Locate every Plasmodium falciparum-infected red blood cell.
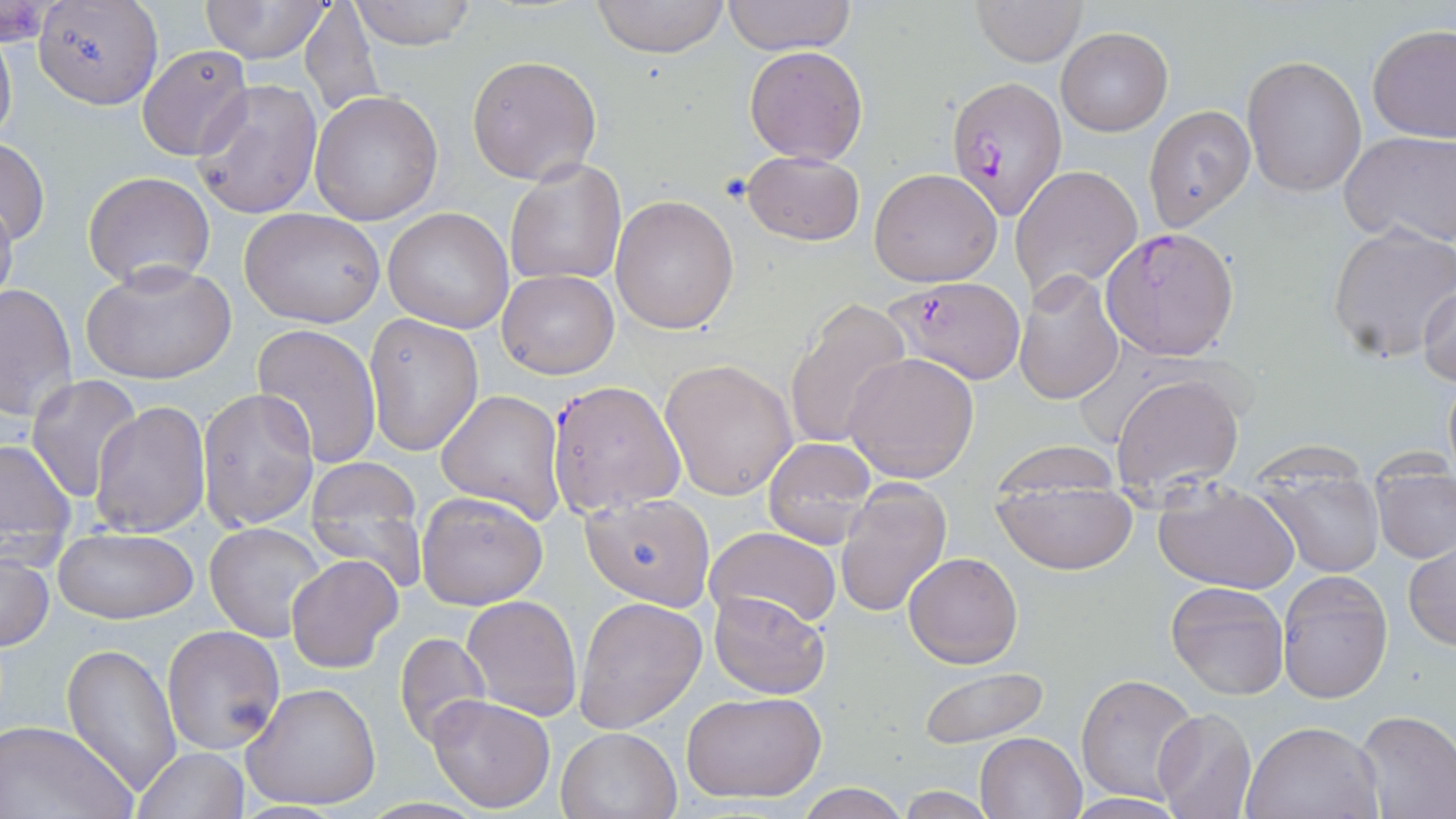

Approximate bounding boxes as named x1/y1/x2/y2 corners in pixels.
Plasmodium falciparum-infected red blood cells: (x1=944, y1=74, x2=1068, y2=220), (x1=1101, y1=226, x2=1241, y2=361), (x1=883, y1=276, x2=1027, y2=385), (x1=547, y1=380, x2=685, y2=516).

Uninfected red blood cell locations: (x1=197, y1=0, x2=333, y2=64), (x1=347, y1=0, x2=478, y2=50), (x1=591, y1=0, x2=731, y2=58), (x1=724, y1=0, x2=856, y2=54), (x1=973, y1=0, x2=1087, y2=66), (x1=33, y1=2, x2=162, y2=109), (x1=298, y1=2, x2=382, y2=116), (x1=0, y1=26, x2=17, y2=157), (x1=1368, y1=26, x2=1456, y2=145), (x1=1056, y1=28, x2=1172, y2=135), (x1=744, y1=45, x2=869, y2=166), (x1=137, y1=46, x2=252, y2=159), (x1=466, y1=54, x2=602, y2=184), (x1=1242, y1=55, x2=1366, y2=197), (x1=192, y1=78, x2=321, y2=219), (x1=310, y1=90, x2=442, y2=226), (x1=1142, y1=105, x2=1255, y2=230), (x1=1340, y1=131, x2=1456, y2=247), (x1=0, y1=138, x2=51, y2=249), (x1=741, y1=149, x2=866, y2=247), (x1=503, y1=156, x2=628, y2=285), (x1=1012, y1=164, x2=1142, y2=300), (x1=869, y1=167, x2=1002, y2=287), (x1=83, y1=171, x2=216, y2=288), (x1=0, y1=185, x2=18, y2=317), (x1=610, y1=195, x2=740, y2=334), (x1=239, y1=207, x2=385, y2=329), (x1=382, y1=207, x2=513, y2=333), (x1=1327, y1=223, x2=1456, y2=363), (x1=81, y1=260, x2=236, y2=385), (x1=495, y1=269, x2=618, y2=380), (x1=1014, y1=269, x2=1124, y2=405), (x1=1, y1=283, x2=77, y2=423), (x1=1418, y1=284, x2=1455, y2=384), (x1=783, y1=297, x2=911, y2=450), (x1=364, y1=312, x2=483, y2=456), (x1=252, y1=324, x2=381, y2=469), (x1=844, y1=352, x2=980, y2=484), (x1=661, y1=359, x2=798, y2=501), (x1=1441, y1=366, x2=1455, y2=484), (x1=1110, y1=371, x2=1244, y2=499), (x1=26, y1=375, x2=143, y2=503), (x1=198, y1=387, x2=319, y2=534), (x1=435, y1=389, x2=566, y2=524), (x1=90, y1=400, x2=211, y2=540), (x1=0, y1=437, x2=76, y2=545), (x1=764, y1=437, x2=881, y2=551), (x1=1364, y1=444, x2=1454, y2=474), (x1=303, y1=457, x2=428, y2=593), (x1=991, y1=459, x2=1139, y2=574), (x1=1261, y1=473, x2=1384, y2=577), (x1=1372, y1=477, x2=1456, y2=563), (x1=836, y1=480, x2=953, y2=618), (x1=1152, y1=481, x2=1299, y2=596), (x1=416, y1=491, x2=548, y2=609), (x1=581, y1=491, x2=715, y2=610), (x1=204, y1=522, x2=327, y2=642), (x1=705, y1=527, x2=840, y2=630), (x1=55, y1=528, x2=198, y2=624), (x1=1404, y1=542, x2=1456, y2=650), (x1=0, y1=551, x2=53, y2=651), (x1=904, y1=551, x2=1023, y2=669), (x1=285, y1=554, x2=403, y2=673), (x1=1277, y1=570, x2=1392, y2=703), (x1=1166, y1=581, x2=1289, y2=700), (x1=708, y1=591, x2=830, y2=699), (x1=461, y1=594, x2=582, y2=720), (x1=575, y1=596, x2=708, y2=733), (x1=162, y1=624, x2=285, y2=755), (x1=394, y1=632, x2=490, y2=749), (x1=61, y1=642, x2=181, y2=798), (x1=917, y1=665, x2=1052, y2=750), (x1=1076, y1=674, x2=1200, y2=804), (x1=243, y1=681, x2=384, y2=812), (x1=681, y1=690, x2=826, y2=804), (x1=427, y1=693, x2=557, y2=814), (x1=1153, y1=707, x2=1257, y2=819), (x1=1352, y1=710, x2=1456, y2=818), (x1=0, y1=719, x2=136, y2=819), (x1=1244, y1=720, x2=1386, y2=819), (x1=557, y1=727, x2=682, y2=818), (x1=975, y1=731, x2=1088, y2=819), (x1=134, y1=747, x2=250, y2=819), (x1=795, y1=782, x2=912, y2=819), (x1=894, y1=785, x2=999, y2=818), (x1=1064, y1=794, x2=1188, y2=818). Slide-level diagnosis: Plasmodium falciparum. Thin blood film. Captured at 1000x magnification. One field of a larger specimen. May-Grünwald-Giemsa-stained preparation. Image is 1456×819 pixels. Optical microscopy.